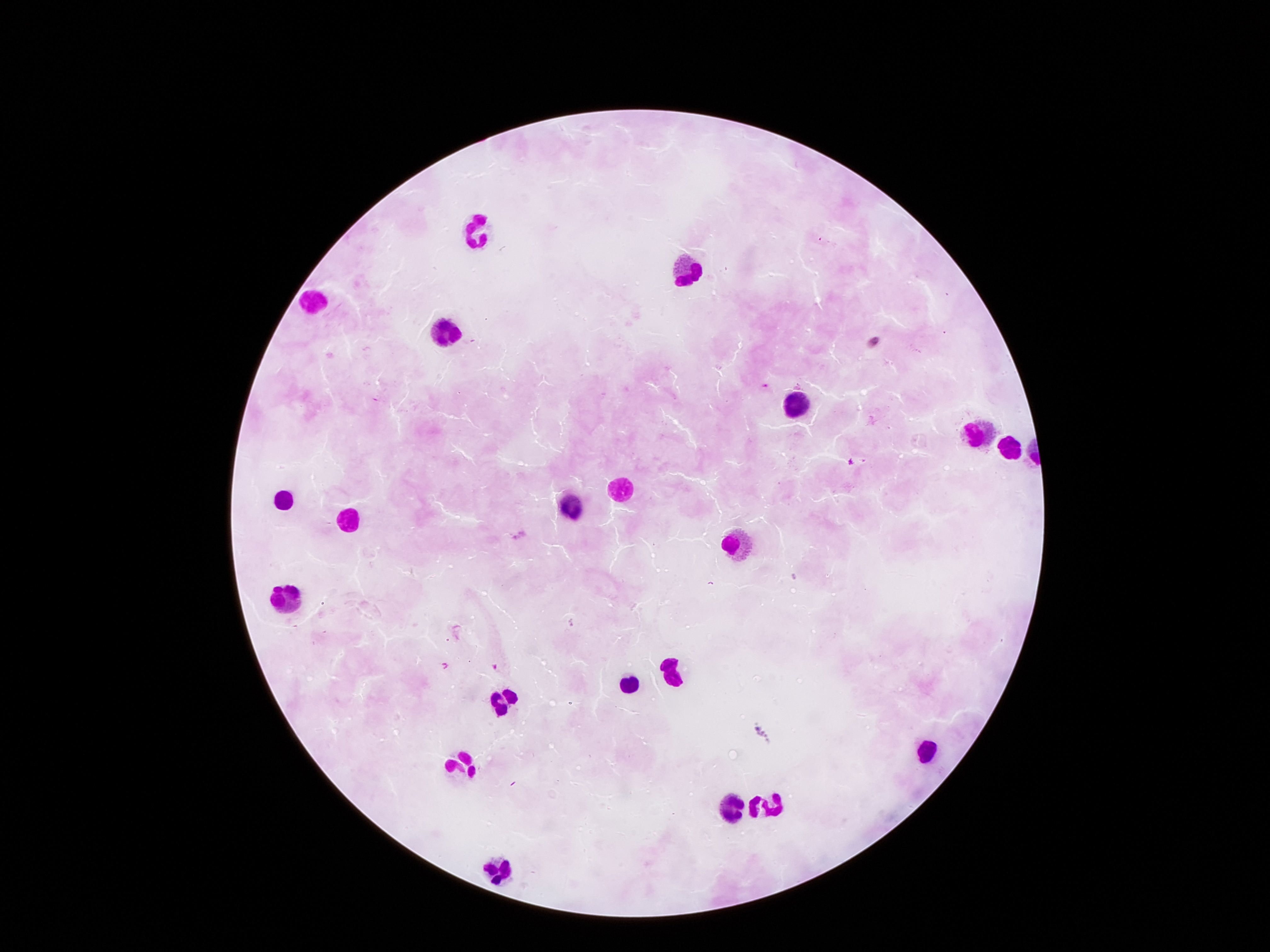 Approximate centers as (x, y) in pixels. Leukocyte locations: (477, 233), (685, 269), (311, 303), (446, 326), (793, 400), (976, 430), (1009, 451), (622, 487), (284, 496), (572, 506), (352, 519), (735, 542), (284, 596), (671, 671), (627, 684), (505, 697), (923, 752), (464, 767), (731, 804), (771, 807), (496, 871). Smartphone photograph taken through the microscope eyepiece. 100x magnification. Patient malaria status: negative. Image is 1270×952 pixels. Giemsa-stained preparation. Thick peripheral-blood smear. One field from this slide.